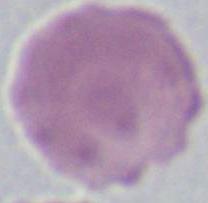

A red blood cell is seen. Captured at 1000x magnification. Micrograph.